Classify this cell by malaria status.
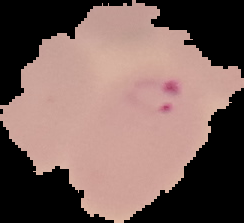

It is parasitized.

The area outside the segmented cell region is set to black. From a thin blood film. Image is 244×223 pixels.